Mark where platelets are.
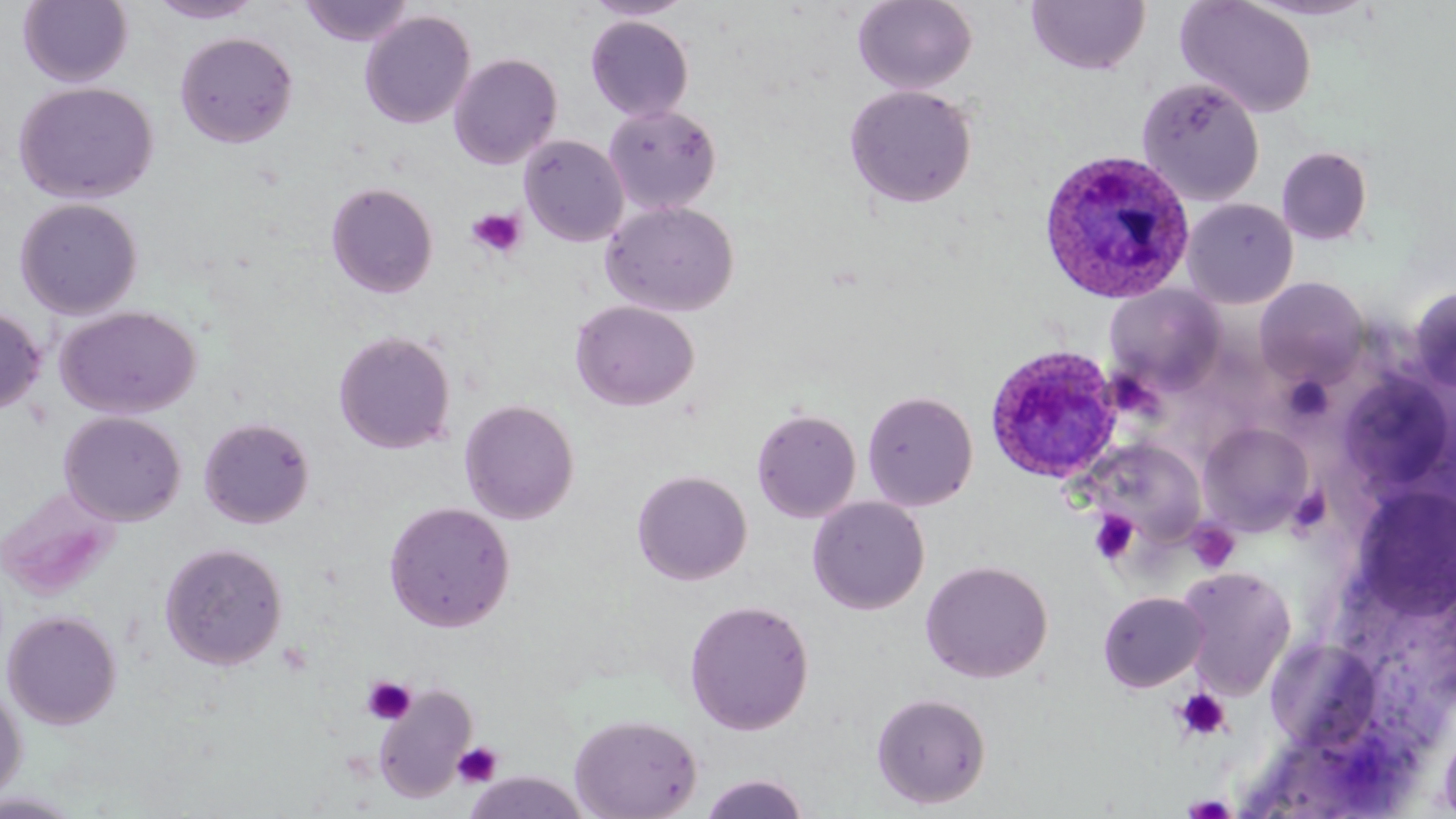

Approximate bounding boxes as (x1, y1, x2, y2) in pixels.
Platelets: (466, 206, 527, 259), (1281, 375, 1335, 425), (1090, 510, 1139, 564), (1188, 520, 1241, 574), (362, 676, 417, 725), (1172, 689, 1232, 741), (452, 741, 503, 788), (1181, 793, 1239, 818).

slide-level diagnosis = Plasmodium ovale
magnification = 1000x
Plasmodium ovale-infected red blood cell locations = approximate bounding boxes as (x1, y1, x2, y2) in pixels: (1037, 148, 1197, 305), (985, 344, 1122, 483)
stain = May-Grünwald-Giemsa
uninfected red blood cell locations = approximate bounding boxes as (x1, y1, x2, y2) in pixels: (18, 0, 133, 87), (299, 0, 415, 47), (582, 0, 696, 21), (852, 0, 978, 94), (1176, 0, 1317, 118), (148, 1, 262, 24), (1026, 1, 1150, 75), (359, 11, 475, 129), (585, 15, 694, 122), (175, 31, 298, 148), (448, 53, 562, 170), (1136, 77, 1265, 205), (13, 82, 158, 204), (843, 84, 978, 209), (603, 103, 722, 215), (519, 135, 628, 247), (1277, 146, 1373, 245), (325, 181, 439, 298), (14, 198, 143, 319), (1182, 198, 1298, 309), (602, 201, 739, 317), (1254, 277, 1368, 387), (1104, 285, 1226, 394), (1408, 286, 1456, 395), (571, 300, 700, 412), (0, 306, 47, 415), (55, 306, 201, 419), (333, 330, 456, 454), (1337, 372, 1455, 496), (862, 389, 978, 511), (459, 399, 580, 524), (751, 408, 862, 523), (59, 411, 187, 526), (198, 417, 315, 529), (1199, 422, 1313, 535), (1081, 438, 1206, 548), (631, 469, 752, 585), (1352, 485, 1456, 619), (0, 488, 122, 600), (807, 496, 930, 615), (383, 501, 515, 633), (159, 542, 288, 670), (919, 560, 1053, 683), (1175, 566, 1296, 699), (1098, 591, 1208, 692), (683, 599, 815, 735), (2, 610, 122, 729), (0, 682, 27, 805), (373, 685, 477, 803), (870, 691, 992, 809), (569, 714, 703, 819), (1438, 716, 1456, 817), (461, 770, 591, 818), (698, 773, 811, 818), (0, 791, 86, 818)
image size = 1456×819 pixels
modality = light microscopy
field of view = one of a larger specimen
preparation = thin blood film